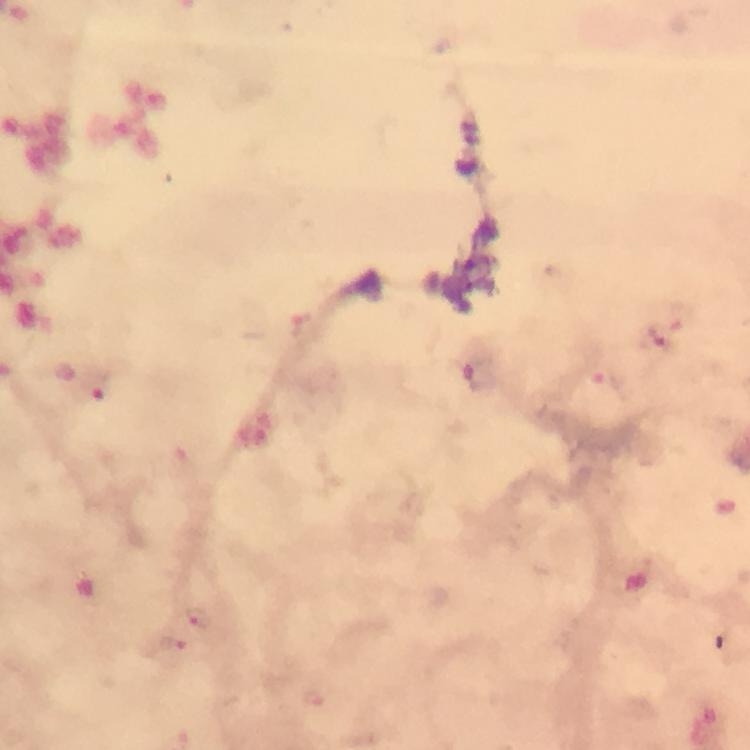
Approximate object centers, in pixels from the top-left corner. Plasmodium parasite locations: (x=676, y=319), (x=301, y=323), (x=479, y=376), (x=600, y=377), (x=92, y=388), (x=198, y=616), (x=172, y=645), (x=316, y=700). Giemsa-stained preparation. A crop from one field of view. 100x magnification. Image is 750×750 pixels. Immersion oil applied. Thick blood film. Photographed with a smartphone mounted on the microscope. From a diagnostic examination for malaria.